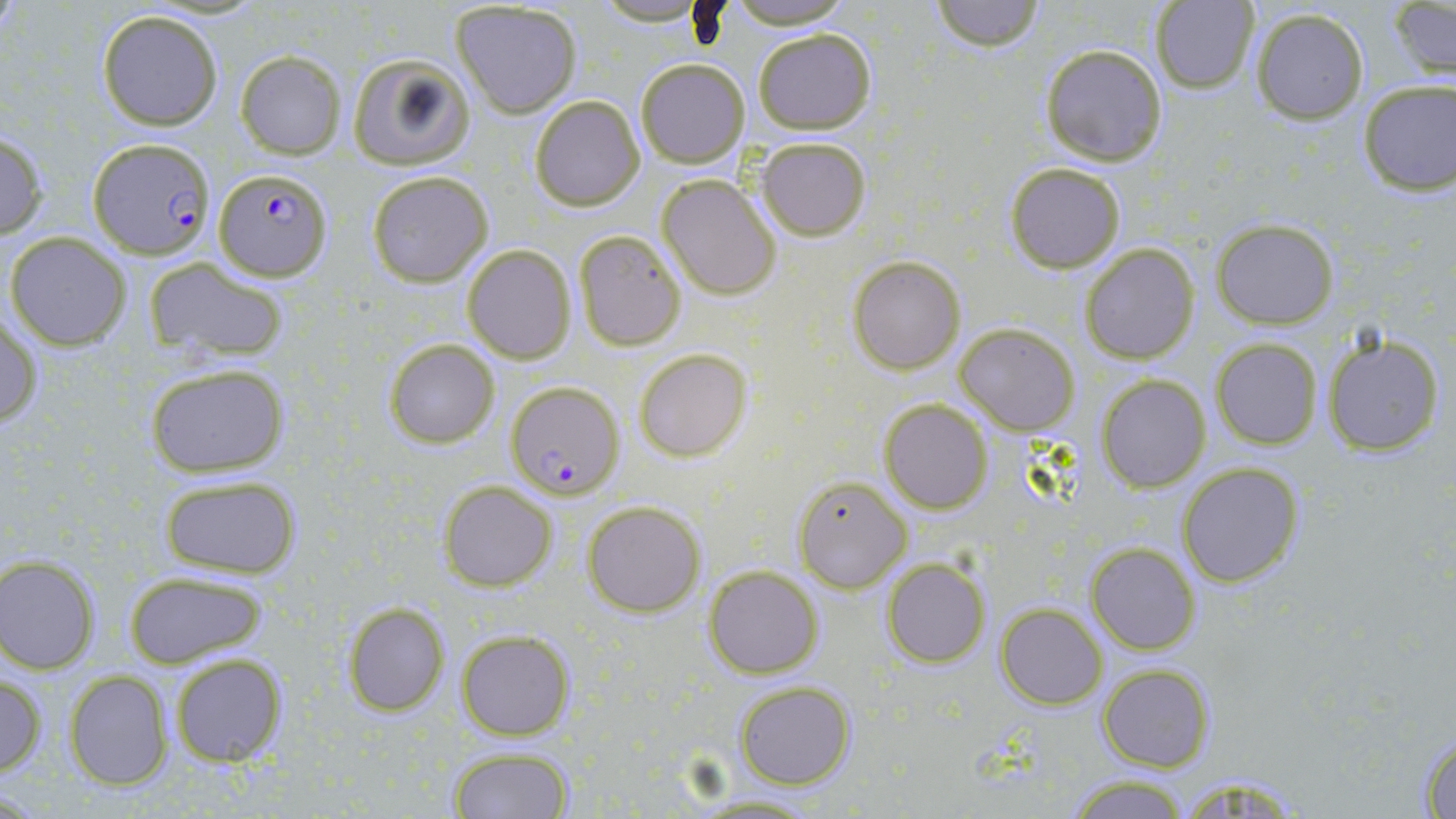

slide-level diagnosis = Plasmodium falciparum
preparation = thin blood film
image size = 1456×819 pixels
uninfected red blood cell locations = approximate bounding boxes as (x1,y1)-(x2,y2) corner pairs in pixels: (592,0)-(711,27), (930,0)-(1045,50), (1149,0)-(1261,94), (721,1)-(861,29), (450,3)-(582,117), (1390,4)-(1455,80), (1248,8)-(1370,125), (97,11)-(224,129), (752,28)-(876,134), (1038,43)-(1168,166), (236,51)-(347,159), (346,53)-(476,171), (635,58)-(749,169), (1356,78)-(1455,196), (529,95)-(645,211), (0,128)-(48,241), (754,137)-(871,240), (1005,163)-(1125,274), (366,170)-(493,286), (656,174)-(782,300), (1212,219)-(1339,329), (573,230)-(685,351), (5,232)-(131,351), (1080,243)-(1199,365), (461,244)-(576,364), (847,255)-(966,374), (142,259)-(286,360), (1,312)-(44,428), (955,322)-(1080,434), (1322,334)-(1444,457), (384,338)-(500,449), (1211,338)-(1322,449), (634,349)-(750,461), (145,362)-(287,477), (1096,374)-(1210,493), (878,399)-(992,514), (1178,463)-(1303,587), (156,473)-(302,580), (793,475)-(911,593), (440,481)-(558,589), (584,500)-(705,618), (1086,542)-(1200,654), (1,555)-(100,673), (882,557)-(990,668), (704,567)-(822,679), (122,571)-(268,670), (342,601)-(451,716), (996,604)-(1106,710), (457,629)-(575,740), (168,652)-(288,767), (1098,663)-(1214,771), (63,670)-(174,790), (0,672)-(47,777), (735,681)-(856,788), (1413,729)-(1456,817), (447,746)-(575,819), (1063,775)-(1192,818)
magnification = 1000x
modality = light microscopy
Plasmodium falciparum-infected red blood cell locations = approximate bounding boxes as (x1,y1)-(x2,y2) corner pairs in pixels: (86,136)-(215,259), (214,168)-(332,280), (506,381)-(623,499)
field of view = one of a larger specimen
stain = May-Grünwald-Giemsa